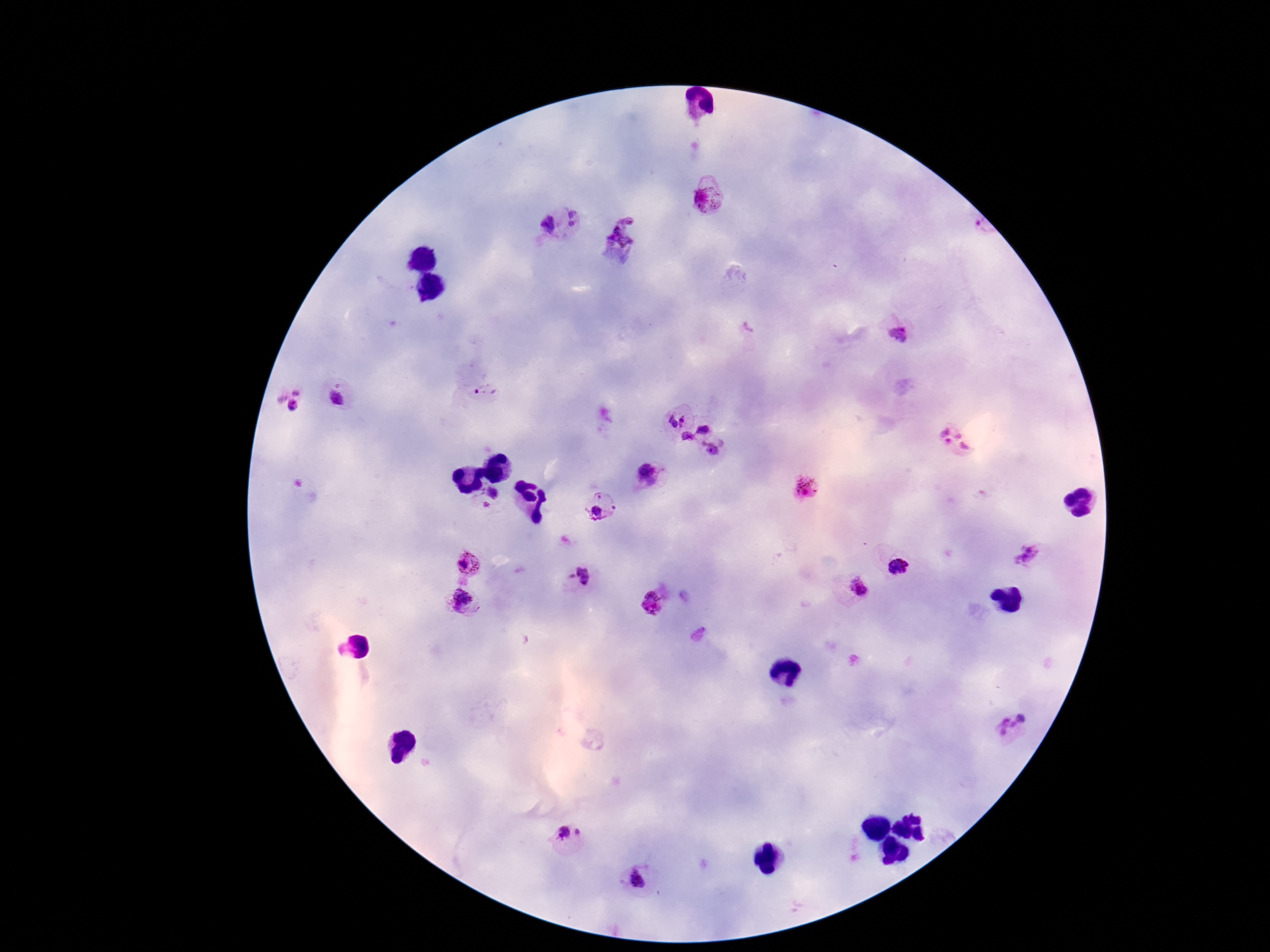 Approximate centers as [x, y] in pixels. Plasmodium parasite locations: [710, 196], [577, 217], [547, 224], [622, 235], [899, 335], [484, 392], [344, 398], [287, 401], [674, 416], [704, 426], [686, 439], [956, 440], [714, 448], [651, 475], [809, 487], [492, 493], [485, 507], [601, 507], [1024, 553], [469, 563], [900, 564], [578, 578], [855, 589], [464, 600], [655, 602], [1013, 725], [572, 834], [637, 881]. Thick peripheral-blood smear. Photographed through the microscope eyepiece with a smartphone camera. Giemsa stain. Single field of view. 100x magnification. Image is 1270×952 pixels. Patient malaria status: positive.